Assess this cell for malaria.
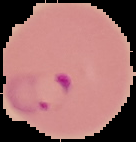
It is parasitized.

image size = 136×142 pixels
image type = segmented cell region with the area outside set to black
preparation = thin blood smear